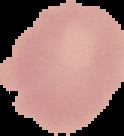

Summary:
  - Image size: 124×136 pixels
  - Image type: segmented cell region on a black background
  - Result: no Plasmodium parasites seen
  - Preparation: thin blood smear